Classify this cell by malaria status.
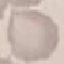

Uninfected.

Summary:
  - Preparation: thin blood smear
  - Image type: cell patch, automatically extracted from a larger field of view and resized to 64 × 64 pixels
  - Capture: smartphone through the microscope eyepiece
  - Stain: Giemsa